Describe the morphology of the red blood cells.
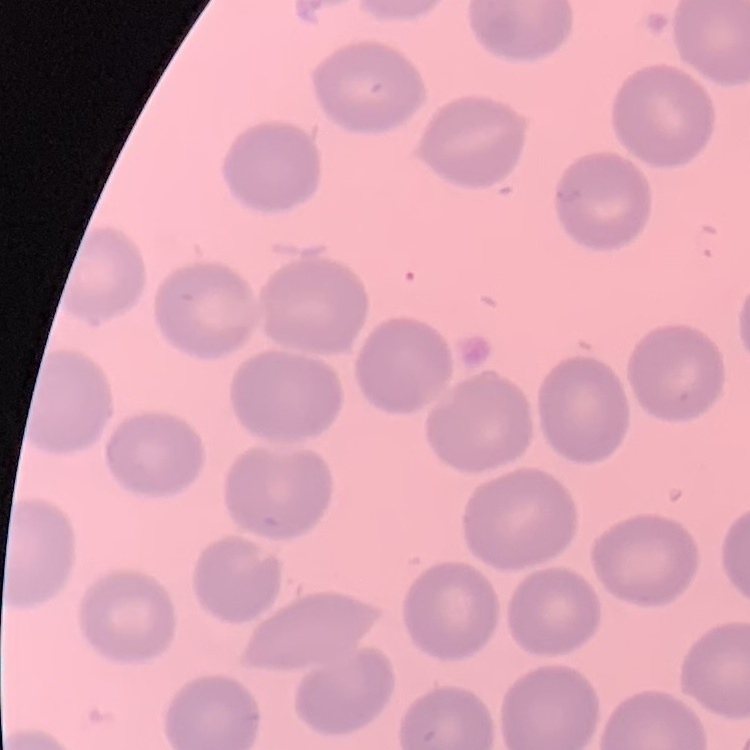

They show no rouleaux formation.

image type = one tile cut from a larger photomicrograph
preparation = thin blood smear
stain = Field's or Giemsa